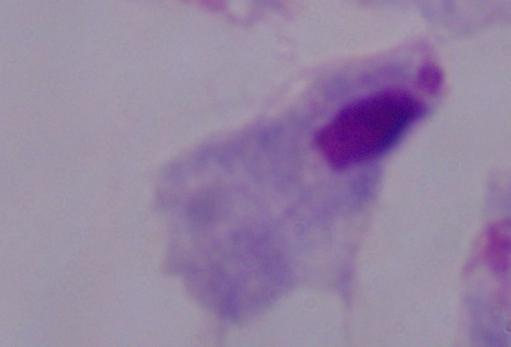

identification = trichomonad
magnification = 1000x
modality = micrograph